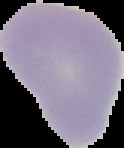

Summary:
  - Image size: 124×148 pixels
  - Image type: segmented cell region with the area outside set to black
  - Preparation: thin blood film
  - Result: no malaria parasites detected